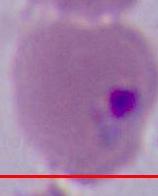 A Plasmodium parasite is shown. Captured at either 400x or 1000x magnification. Micrograph.